Locate every Plasmodium parasite.
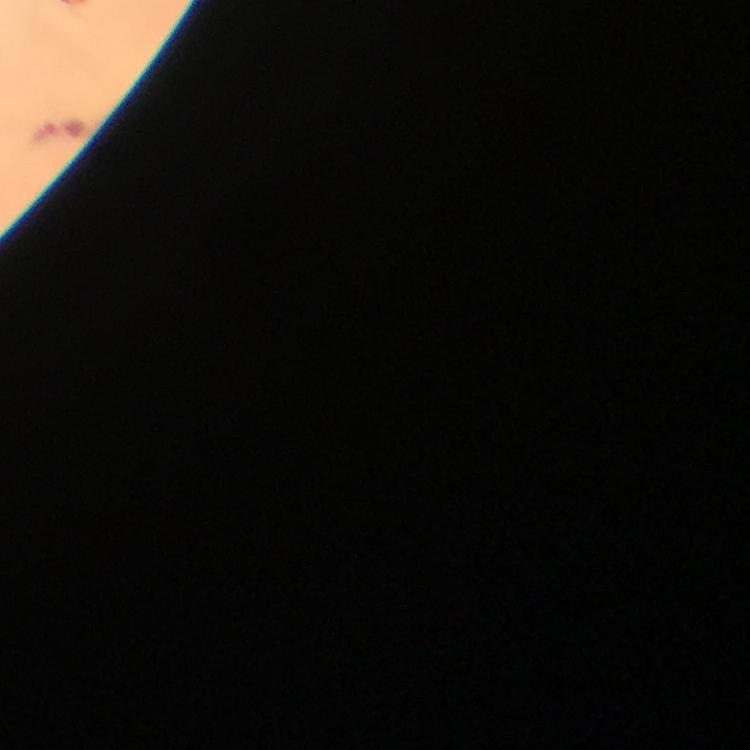
Approximate object centers, in pixels from the top-left corner.
Plasmodium parasites: (x=61, y=130).

cropped from = one field of view
magnification = 100x
preparation = thick blood film
immersion oil = used
capture = smartphone photograph through a microscope
image size = 750×750 pixels
stain = Giemsa
context = from a malaria diagnostic workup